Give the extent of all uninfected red blood cells.
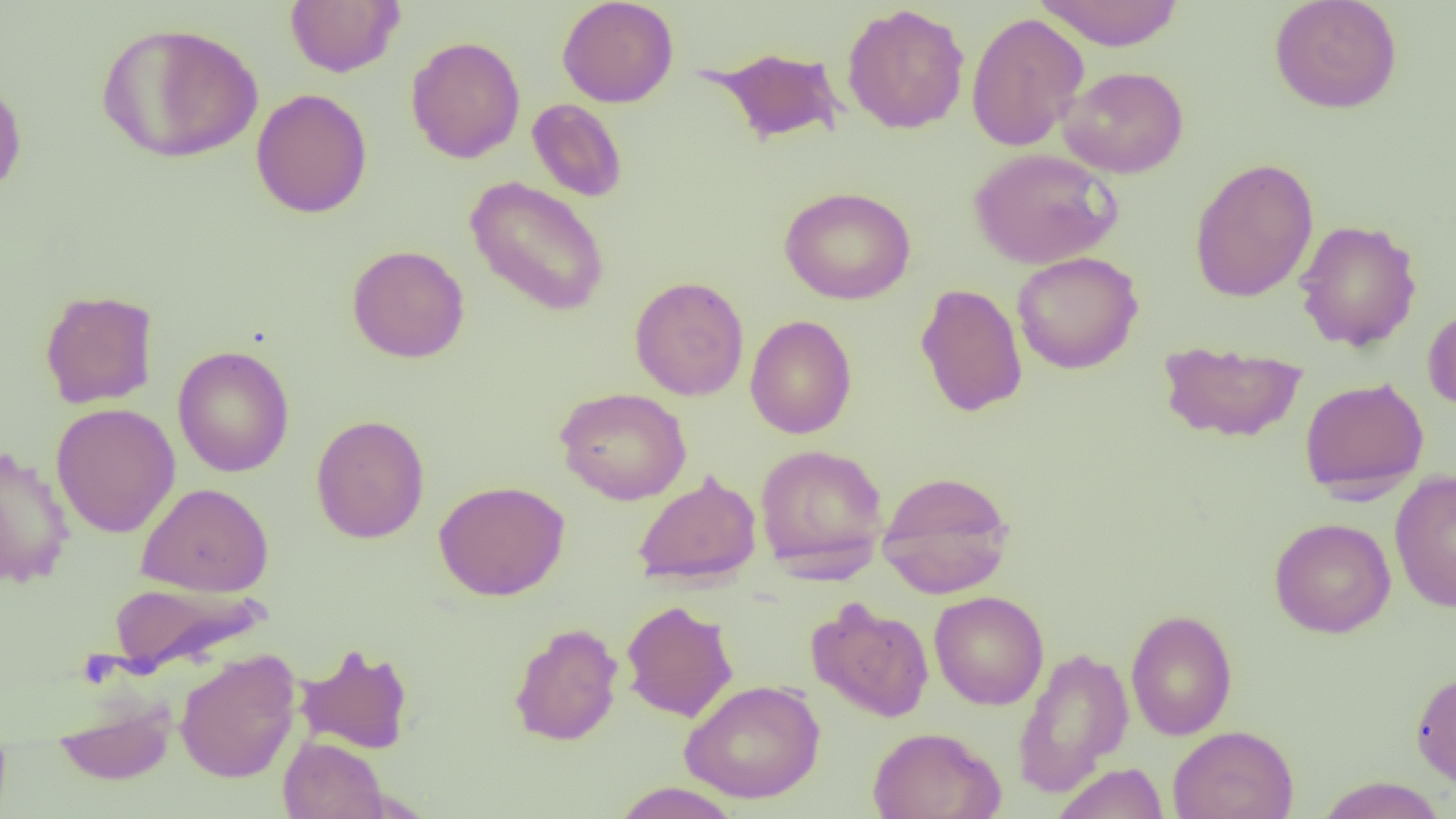
Approximate bounding boxes as named x1/y1/x2/y2 corners in pixels.
Uninfected red blood cells: (x1=285, y1=0, x2=404, y2=77), (x1=557, y1=0, x2=679, y2=108), (x1=1034, y1=0, x2=1185, y2=50), (x1=1268, y1=0, x2=1402, y2=114), (x1=842, y1=4, x2=970, y2=134), (x1=966, y1=12, x2=1089, y2=152), (x1=96, y1=23, x2=264, y2=164), (x1=406, y1=36, x2=525, y2=163), (x1=703, y1=45, x2=846, y2=146), (x1=1060, y1=66, x2=1189, y2=178), (x1=0, y1=76, x2=27, y2=201), (x1=251, y1=88, x2=373, y2=219), (x1=527, y1=98, x2=628, y2=202), (x1=969, y1=147, x2=1121, y2=269), (x1=1189, y1=157, x2=1319, y2=303), (x1=464, y1=176, x2=611, y2=318), (x1=779, y1=186, x2=916, y2=305), (x1=1294, y1=219, x2=1422, y2=351), (x1=346, y1=244, x2=470, y2=363), (x1=1011, y1=251, x2=1143, y2=374), (x1=629, y1=275, x2=749, y2=401), (x1=915, y1=283, x2=1028, y2=418), (x1=39, y1=289, x2=159, y2=408), (x1=1423, y1=306, x2=1456, y2=411), (x1=744, y1=314, x2=857, y2=438), (x1=1157, y1=339, x2=1307, y2=443), (x1=172, y1=345, x2=294, y2=478), (x1=1300, y1=377, x2=1429, y2=498), (x1=555, y1=387, x2=692, y2=505), (x1=51, y1=402, x2=180, y2=538), (x1=311, y1=414, x2=429, y2=543), (x1=754, y1=443, x2=889, y2=576), (x1=0, y1=444, x2=75, y2=589), (x1=632, y1=470, x2=762, y2=587), (x1=876, y1=470, x2=1015, y2=598), (x1=1390, y1=470, x2=1456, y2=613), (x1=433, y1=480, x2=570, y2=601), (x1=136, y1=482, x2=274, y2=596), (x1=1269, y1=517, x2=1396, y2=638), (x1=106, y1=579, x2=272, y2=674), (x1=929, y1=590, x2=1049, y2=710), (x1=806, y1=597, x2=934, y2=723), (x1=621, y1=600, x2=738, y2=722), (x1=1125, y1=609, x2=1238, y2=740), (x1=509, y1=622, x2=624, y2=746), (x1=295, y1=643, x2=414, y2=754), (x1=1012, y1=646, x2=1133, y2=797), (x1=175, y1=650, x2=302, y2=784), (x1=1411, y1=667, x2=1456, y2=788), (x1=679, y1=679, x2=826, y2=803), (x1=53, y1=695, x2=177, y2=786), (x1=1167, y1=725, x2=1299, y2=819), (x1=867, y1=727, x2=1005, y2=819), (x1=278, y1=736, x2=389, y2=819), (x1=1053, y1=763, x2=1169, y2=819), (x1=1315, y1=776, x2=1449, y2=819), (x1=611, y1=782, x2=744, y2=819).

Summary:
  - Slide-level diagnosis: no evidence of blood parasites
  - Magnification: 1000x
  - Image size: 1456×819 pixels
  - Preparation: thin blood smear
  - Modality: light microscopy
  - Field of view: one of a larger specimen